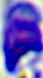
{
  "modality": "photomicrograph",
  "identification": "leukocyte",
  "magnification": "400x"
}